Point out each Plasmodium parasite and each leukocyte.
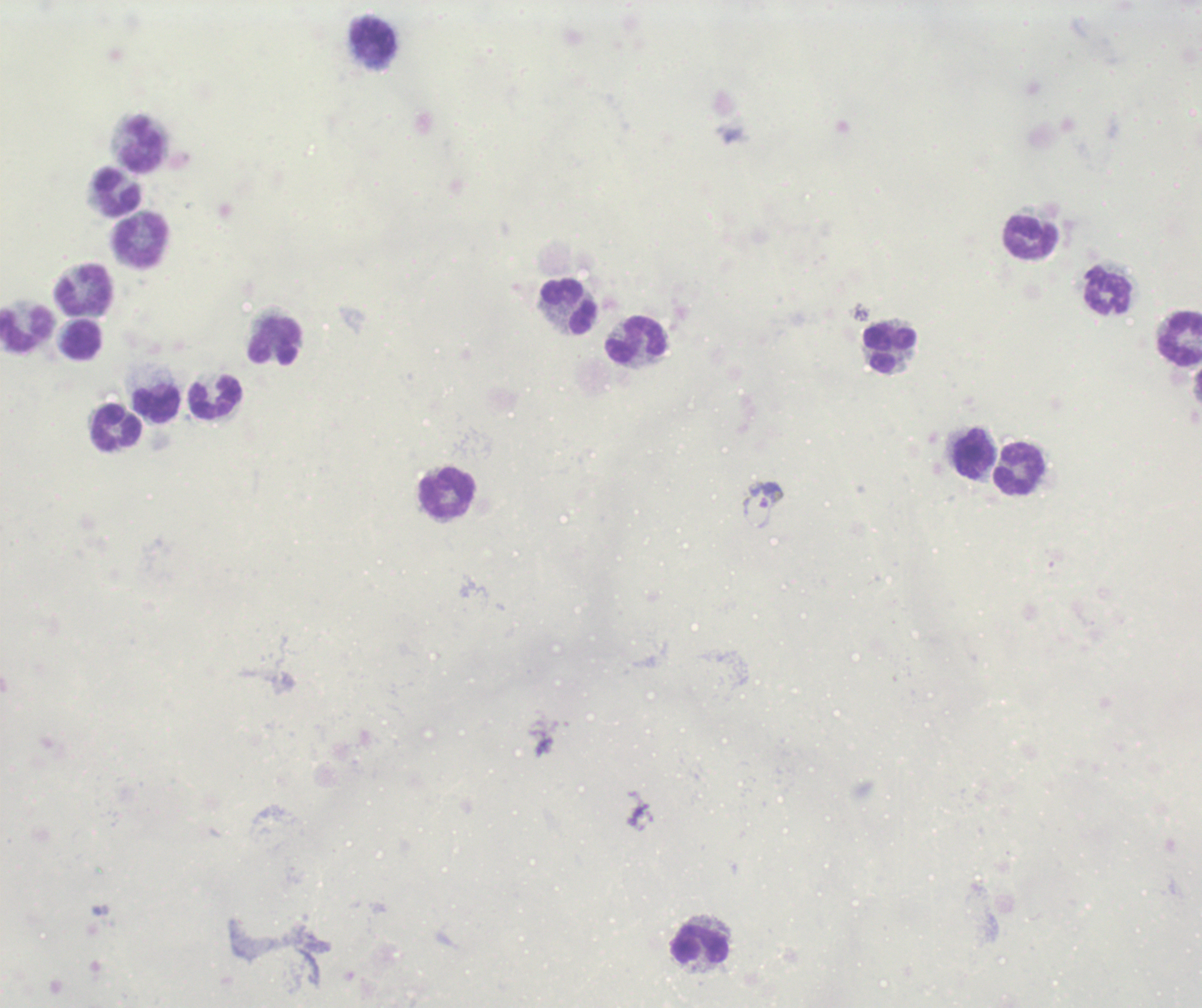

Approximate centers as [x, y] in pixels.
Gametocytes: [763, 506].
No trophozoite or schizont forms observed.
Leukocytes: [374, 42], [144, 145], [118, 191], [1032, 237], [141, 241], [84, 290], [1108, 291], [568, 307], [26, 330], [1180, 337], [637, 339], [83, 340], [276, 342], [890, 349], [216, 398], [157, 406], [117, 427], [974, 454], [1019, 469], [447, 494], [700, 945].

field_of_view: one from this slide
background_quality: unsatisfactory
magnification: 100x
image_size: 1202×1008 pixels
stain: Romanowsky
preparation: thick smear of blood
context: previously used in a real diagnosis